Locate every Plasmodium ovale-infected red blood cell.
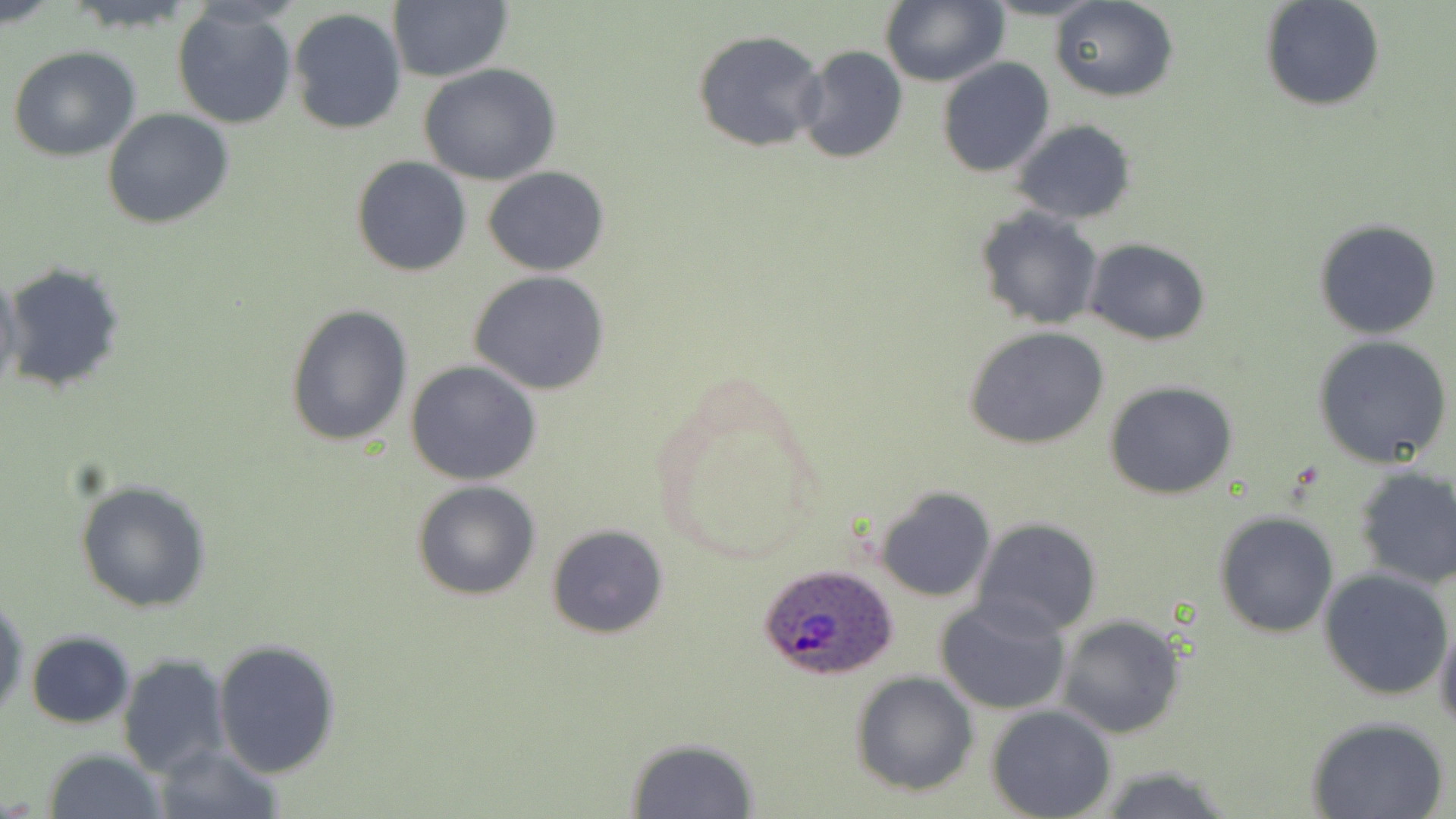
Approximate bounding boxes as (x1,y1)-(x2,y2) corner pairs in pixels.
Plasmodium ovale-infected red blood cells: (759,563)-(899,680).

Summary:
  - Uninfected red blood cell locations: (1,0)-(60,28), (880,0)-(1006,87), (1051,0)-(1177,101), (1259,0)-(1386,111), (388,2)-(513,82), (173,5)-(298,129), (288,8)-(409,137), (692,29)-(826,153), (8,45)-(141,161), (796,46)-(907,164), (937,57)-(1055,178), (418,63)-(561,185), (102,108)-(234,229), (1012,119)-(1137,225), (351,156)-(472,277), (483,166)-(610,276), (975,207)-(1103,331), (1314,219)-(1442,338), (1086,239)-(1211,345), (1,260)-(126,395), (0,263)-(23,402), (469,270)-(610,394), (285,304)-(413,448), (964,326)-(1109,449), (1312,335)-(1456,469), (405,361)-(543,486), (1105,380)-(1238,499), (1352,466)-(1456,591), (74,479)-(213,613), (413,481)-(541,601), (874,487)-(996,603), (1214,511)-(1339,638), (974,518)-(1100,636), (545,525)-(669,640), (1318,567)-(1456,701), (0,594)-(28,721), (937,598)-(1071,716), (1057,615)-(1186,738), (1435,617)-(1456,738), (25,632)-(136,729), (214,640)-(342,778), (117,652)-(231,779), (850,672)-(978,795), (987,705)-(1116,819), (1306,715)-(1450,819), (624,738)-(760,819), (150,742)-(282,818), (44,748)-(165,819), (1095,765)-(1235,819)
  - Slide-level diagnosis: Plasmodium ovale
  - Modality: light microscopy
  - Field of view: one of a larger specimen
  - Preparation: thin blood smear
  - Stain: May-Grünwald-Giemsa
  - Magnification: 1000x
  - Image size: 1456×819 pixels